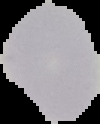

Cell region segmented out of the field of view; the surrounding area is masked to black. Malaria status: uninfected. From a thin blood smear. Image is 100×124 pixels.